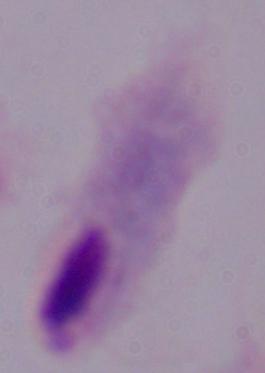
identification = trichomonad
modality = micrograph
magnification = 1000x